Report the malaria status of this cell.
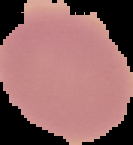
Uninfected.

image type = segmented cell region on a black background
image size = 133×145 pixels
preparation = thin blood film